Name the blood parasite species.
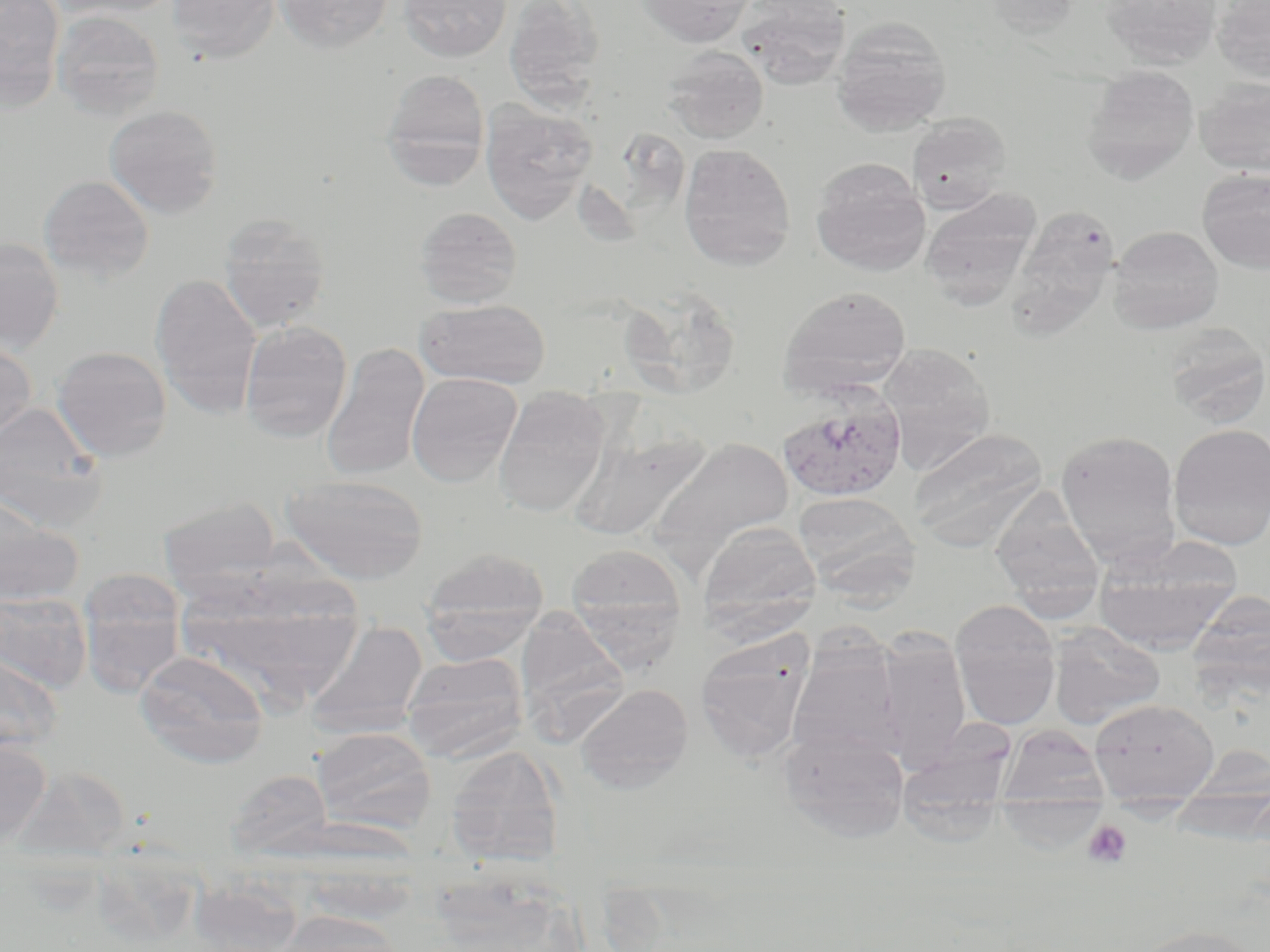

Plasmodium vivax.

Approximate bounding boxes as [x1, y1, x2, y2] in pixels. Uninfected red blood cell locations: [0, 0, 66, 110], [48, 0, 182, 19], [168, 0, 280, 63], [275, 0, 394, 52], [398, 0, 512, 62], [503, 0, 605, 110], [638, 0, 755, 47], [737, 0, 852, 88], [981, 0, 1081, 37], [1100, 0, 1223, 69], [1212, 0, 1270, 83], [51, 10, 165, 120], [831, 18, 952, 134], [662, 46, 769, 144], [1080, 67, 1200, 184], [381, 68, 490, 186], [1195, 77, 1270, 176], [480, 101, 596, 224], [104, 104, 224, 218], [907, 113, 1012, 214], [678, 143, 796, 270], [810, 157, 931, 276], [1197, 168, 1270, 274], [38, 175, 154, 283], [919, 189, 1041, 308], [414, 206, 523, 308], [1016, 206, 1113, 338], [217, 213, 331, 332], [1108, 225, 1224, 334], [0, 237, 65, 354], [150, 273, 262, 418], [778, 285, 912, 398], [626, 286, 739, 401], [415, 299, 551, 389], [240, 320, 352, 442], [1161, 324, 1270, 427], [0, 339, 37, 442], [876, 343, 996, 470], [321, 344, 430, 482], [51, 346, 172, 462], [406, 372, 522, 487], [492, 386, 611, 519], [0, 402, 108, 531], [569, 422, 711, 543], [1167, 423, 1270, 550], [908, 427, 1047, 551], [1055, 430, 1183, 567], [647, 436, 795, 573], [282, 474, 429, 584], [990, 486, 1105, 617], [794, 490, 920, 603], [0, 494, 84, 607], [157, 497, 282, 596], [696, 521, 820, 639], [1091, 541, 1242, 655], [566, 543, 686, 652], [420, 548, 549, 660], [78, 571, 187, 698], [175, 576, 364, 709], [1187, 590, 1270, 702], [0, 591, 93, 692], [950, 599, 1061, 729], [513, 605, 630, 737], [307, 620, 428, 738], [1048, 623, 1165, 729], [877, 630, 972, 768], [694, 631, 815, 764], [788, 641, 903, 760], [0, 649, 64, 753], [134, 650, 269, 768], [401, 652, 529, 761], [575, 683, 694, 793], [1089, 698, 1219, 802], [911, 709, 1013, 851], [998, 724, 1109, 808], [313, 726, 436, 833], [778, 727, 911, 843], [0, 739, 52, 849], [445, 745, 564, 866], [12, 765, 132, 863], [226, 768, 334, 862], [306, 818, 417, 920], [189, 877, 301, 951], [272, 911, 408, 952], [1124, 924, 1268, 952]. Plasmodium vivax-infected red blood cell locations: [776, 391, 907, 502]. Platelet locations: [1082, 819, 1133, 869]. Single field of view. Light microscopy. May-Grünwald-Giemsa-stained preparation. Image is 1270×952 pixels. 1000x magnification. Thin blood smear.